Outline each Plasmodium malariae-infected red blood cell.
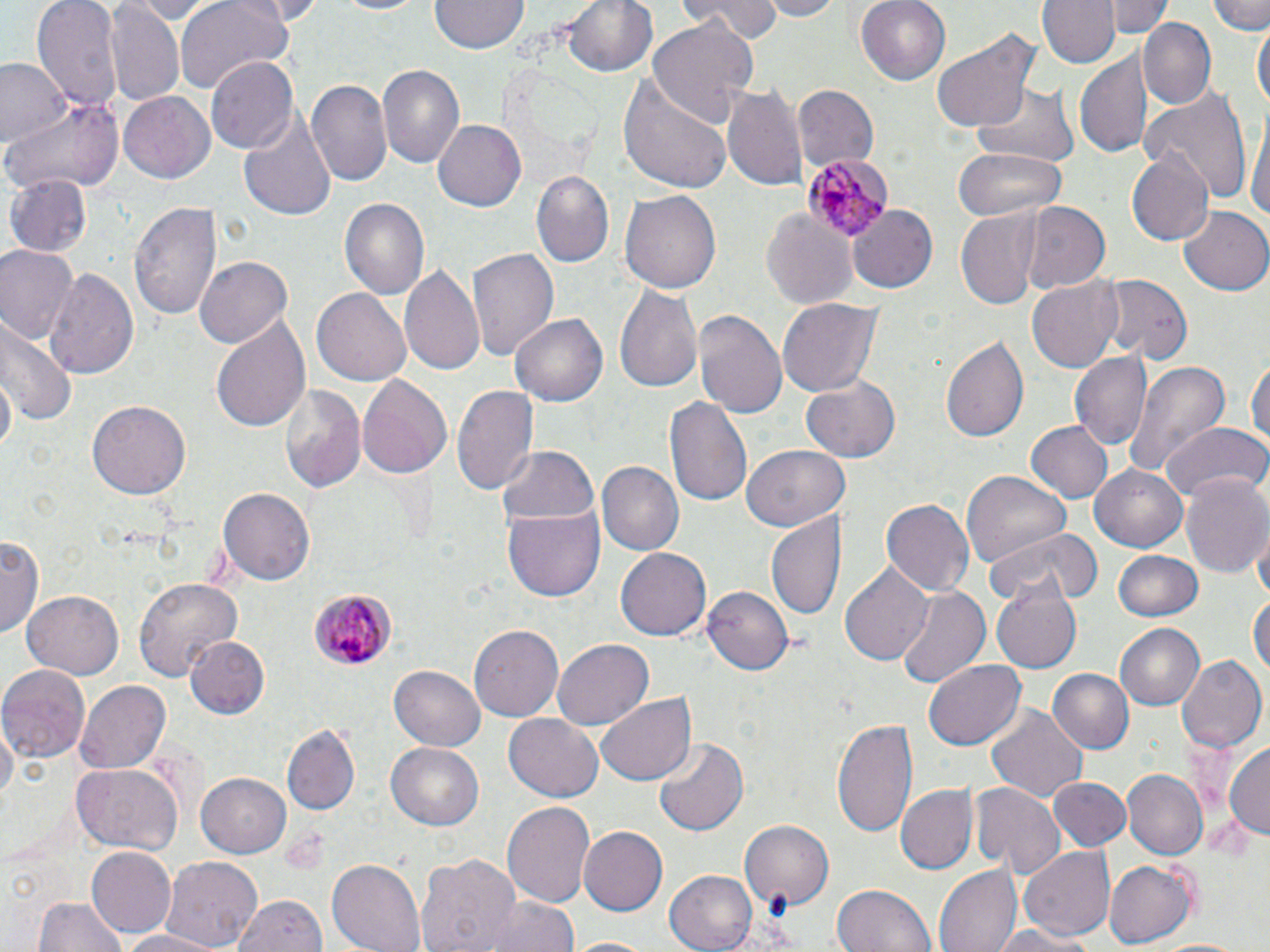

Approximate bounding boxes as (x1,y1)-(x2,y2) corner pairs in pixels.
Plasmodium malariae-infected red blood cells: (802,153)-(892,239), (308,586)-(397,672).

Summary:
  - Uninfected red blood cell locations: (34,0)-(121,114), (120,0)-(219,22), (176,0)-(292,91), (334,0)-(435,17), (562,0)-(659,79), (682,0)-(781,43), (759,0)-(845,20), (856,0)-(950,86), (1035,0)-(1118,69), (1109,0)-(1169,37), (1208,0)-(1268,34), (107,1)-(183,106), (429,2)-(525,55), (1243,8)-(1270,90), (649,17)-(757,131), (1140,19)-(1216,109), (1252,19)-(1269,116), (931,26)-(1039,133), (1076,49)-(1151,158), (2,57)-(70,149), (207,58)-(298,155), (376,66)-(465,169), (620,70)-(733,193), (307,80)-(393,186), (725,80)-(808,195), (973,81)-(1079,167), (792,85)-(878,170), (1143,88)-(1255,206), (118,93)-(215,185), (5,95)-(124,196), (238,108)-(337,222), (1249,109)-(1270,234), (432,119)-(527,213), (952,146)-(1063,221), (1126,150)-(1214,246), (531,170)-(615,268), (4,174)-(91,257), (619,189)-(722,295), (340,198)-(429,302), (130,201)-(221,325), (1022,201)-(1111,294), (849,205)-(939,294), (1180,205)-(1270,296), (761,208)-(857,309), (957,212)-(1048,309), (467,244)-(559,361), (0,247)-(78,346), (197,254)-(293,347), (399,264)-(487,377), (43,266)-(140,380), (1096,275)-(1192,364), (1026,276)-(1123,374), (613,286)-(703,397), (312,287)-(411,386), (776,297)-(882,399), (692,308)-(788,421), (511,313)-(608,407), (209,314)-(310,435), (1,318)-(78,432), (942,335)-(1033,443), (1071,352)-(1149,449), (1248,353)-(1269,457), (1119,360)-(1230,479), (1,366)-(17,459), (356,372)-(455,482), (801,375)-(902,463), (452,381)-(537,495), (279,383)-(368,495), (665,394)-(754,511), (89,400)-(190,499), (1025,421)-(1114,504), (1161,423)-(1267,507), (495,446)-(598,528), (740,446)-(850,533), (596,462)-(684,554), (1089,462)-(1189,553), (961,473)-(1071,570), (1180,473)-(1269,578), (218,488)-(312,586), (883,499)-(974,598), (504,508)-(604,600), (766,514)-(847,623), (984,525)-(1098,611), (1,532)-(43,641), (1253,534)-(1270,603), (616,548)-(711,641), (1114,550)-(1202,622), (838,563)-(933,667), (133,576)-(242,684), (995,583)-(1080,672), (703,586)-(794,675), (895,587)-(990,686), (23,590)-(123,679), (1250,590)-(1269,682), (1115,623)-(1206,711), (470,625)-(563,721), (187,637)-(269,716), (553,637)-(655,730), (1175,652)-(1266,752), (925,660)-(1026,750), (0,664)-(91,759), (390,665)-(485,751), (1045,668)-(1134,754), (75,679)-(170,774), (595,694)-(693,785), (987,704)-(1088,804), (505,712)-(603,802), (2,716)-(17,809), (834,718)-(918,836), (283,725)-(359,814), (651,737)-(749,838), (1225,741)-(1270,842), (387,742)-(483,828), (73,764)-(182,854), (1122,770)-(1207,861), (197,771)-(293,858), (1048,777)-(1130,851), (970,782)-(1065,878), (898,786)-(977,874), (501,800)-(595,911), (740,819)-(834,916), (579,825)-(668,917), (1019,846)-(1116,942), (87,848)-(176,938), (415,853)-(522,952), (163,856)-(262,949), (325,858)-(426,952), (1104,858)-(1196,948), (935,865)-(1021,952), (665,868)-(760,952), (831,883)-(938,952), (232,893)-(326,952), (483,895)-(580,952), (34,896)-(127,952), (981,922)-(1101,951), (110,928)-(232,951), (565,936)-(661,952), (1150,937)-(1254,952)
  - Slide-level diagnosis: Plasmodium malariae
  - Stain: May-Grünwald-Giemsa
  - Magnification: 1000x
  - Field of view: single
  - Modality: optical microscopy
  - Preparation: thin blood smear
  - Image size: 1270×952 pixels